Classify this cell by malaria status.
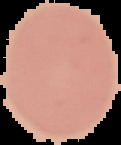

It is uninfected.

{
  "image_size": "121×145 pixels",
  "image_type": "segmented cell region on a black background",
  "preparation": "thin blood smear"
}